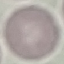
malaria status = uninfected
image type = automatically extracted cell patch, resized to 64 × 64 pixels
capture = smartphone through the microscope eyepiece
preparation = thin blood film
stain = Giemsa